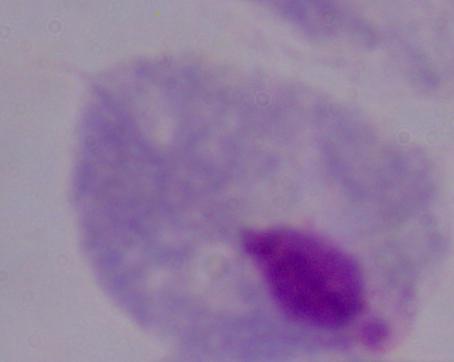

A trichomonad is seen. Photomicrograph. 1000x magnification.